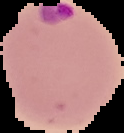 Image is 124×133 pixels. From a thin blood smear. Segmented cell region on a black background. Result: malaria parasites identified.